Report the malaria status.
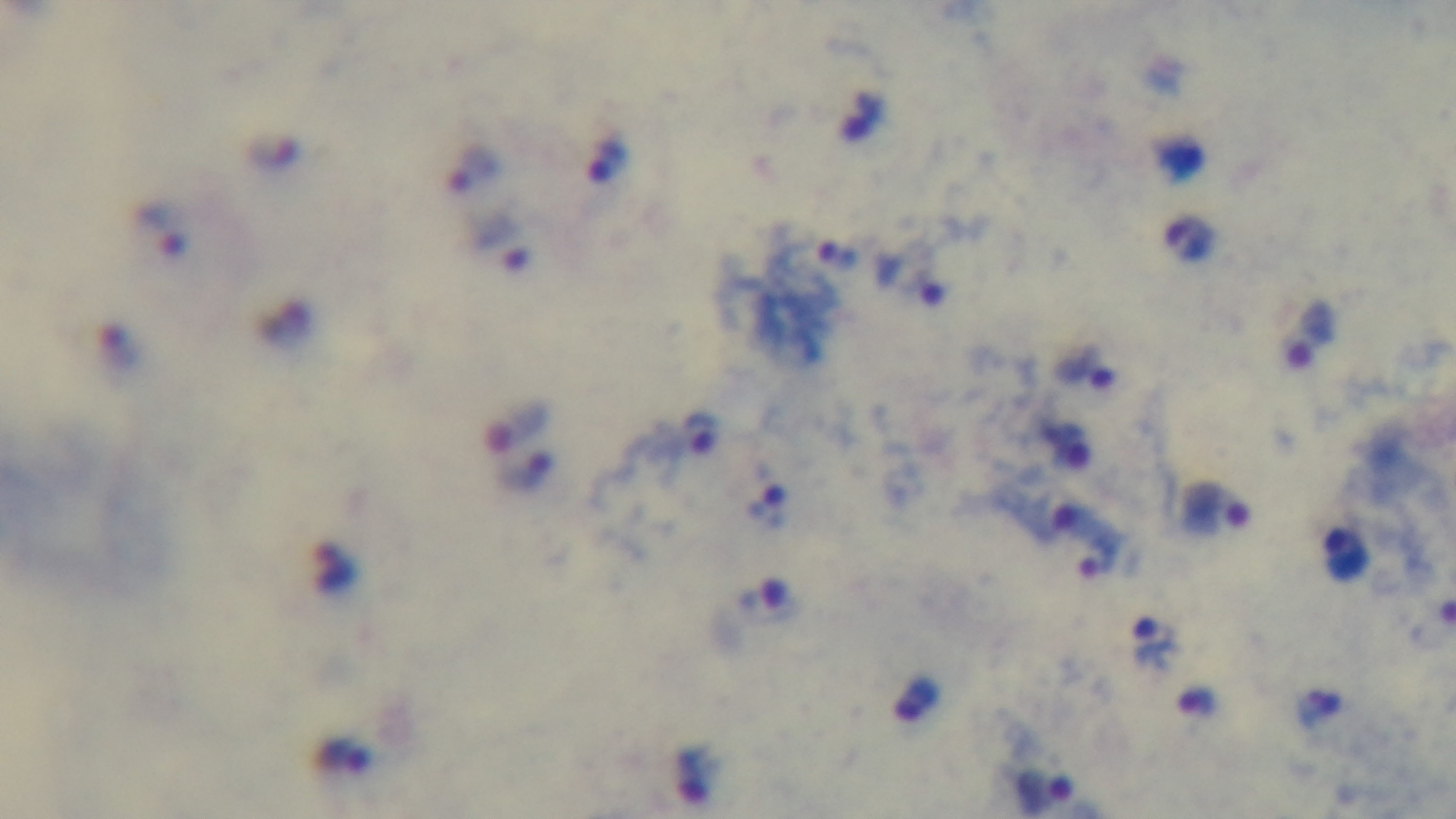

Infected.

Summary:
  - Field of view: single
  - Capture: mounted 4K digital camera
  - Stain: Giemsa
  - Preparation: thick smear
  - Objective: 100x oil immersion
  - Modality: light microscopy